Outline each uninfected red blood cell.
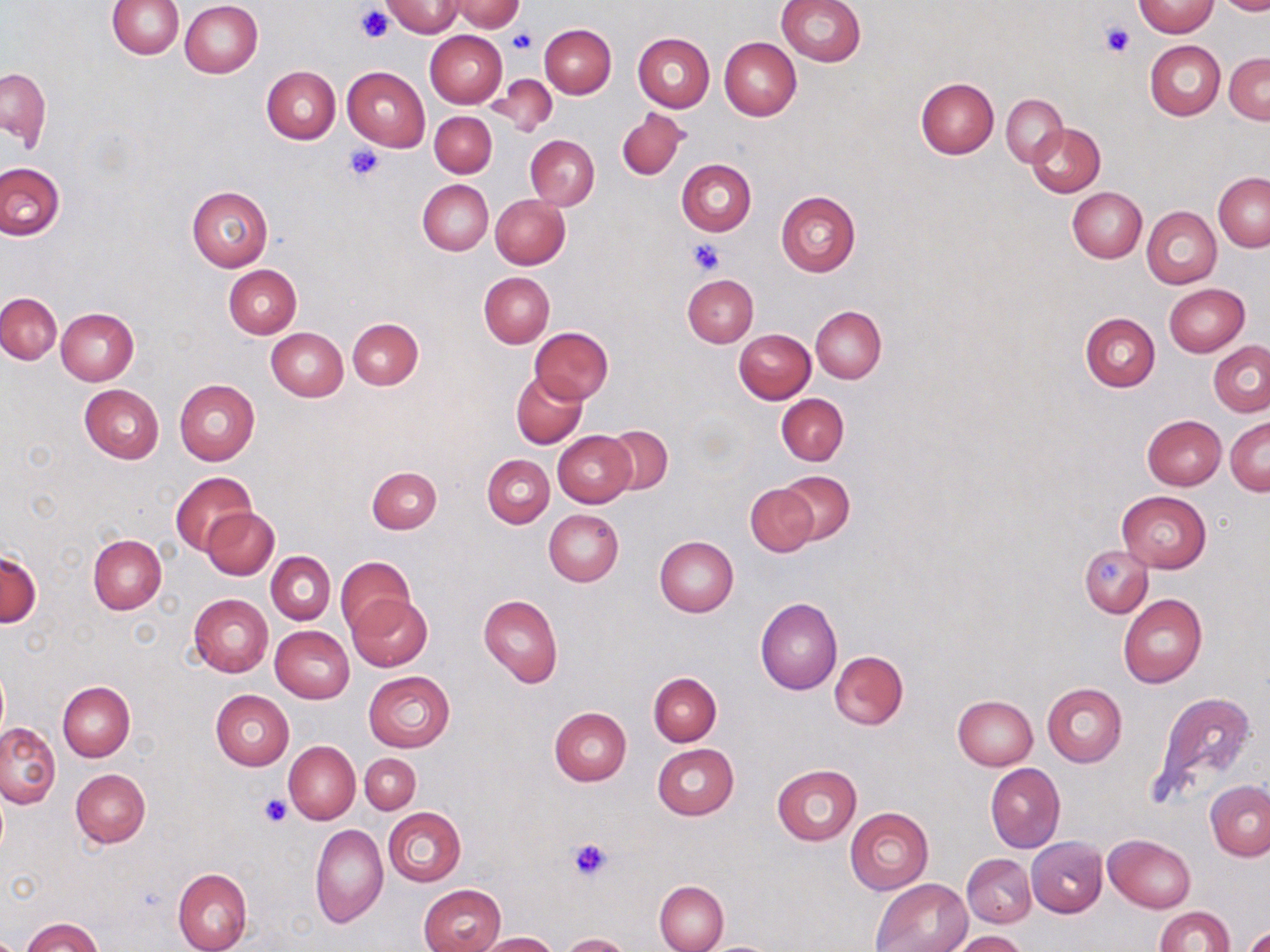

Approximate bounding boxes as (x1,y1)-(x2,y2) corner pairs in pixels.
Uninfected red blood cells: (108,0)-(184,59), (776,0)-(866,65), (1213,0)-(1270,15), (180,1)-(263,78), (382,1)-(463,36), (450,1)-(527,32), (1133,2)-(1218,37), (540,23)-(615,97), (424,30)-(506,108), (632,32)-(715,112), (719,38)-(801,120), (1146,41)-(1225,120), (1225,52)-(1270,124), (262,66)-(340,144), (342,66)-(430,151), (1,68)-(50,148), (488,75)-(558,137), (915,77)-(998,158), (1002,93)-(1067,166), (616,108)-(689,180), (429,111)-(496,177), (1028,122)-(1105,196), (526,135)-(599,209), (677,159)-(756,235), (0,162)-(65,240), (1213,173)-(1270,252), (418,180)-(493,255), (187,185)-(273,272), (1067,187)-(1146,263), (776,190)-(861,276), (489,194)-(571,269), (1142,206)-(1222,289), (224,264)-(301,338), (479,271)-(555,348), (682,274)-(758,347), (1164,284)-(1250,357), (0,293)-(61,364), (811,306)-(886,383), (56,307)-(139,384), (1080,312)-(1160,391), (348,318)-(424,390), (530,327)-(612,403), (266,328)-(348,401), (735,329)-(815,403), (1208,340)-(1270,416), (510,372)-(586,448), (174,379)-(260,464), (79,384)-(164,463), (776,393)-(849,465), (1142,414)-(1226,490), (1227,417)-(1269,495), (603,425)-(672,495), (552,431)-(636,507), (482,453)-(555,527), (367,466)-(442,534), (170,471)-(257,556), (778,471)-(854,544), (745,482)-(819,557), (1116,490)-(1211,572), (203,507)-(279,579), (544,509)-(623,586), (88,534)-(166,614), (654,535)-(738,617), (1078,545)-(1154,618), (0,549)-(40,627), (266,551)-(335,625), (335,556)-(416,635), (189,594)-(273,678), (347,594)-(433,671), (478,594)-(562,688), (1118,594)-(1207,688), (755,597)-(842,694), (270,625)-(354,702), (829,650)-(908,730), (0,667)-(8,740), (364,671)-(454,752), (649,672)-(721,745), (58,682)-(134,760), (1042,683)-(1127,766), (210,689)-(294,770), (1146,689)-(1258,808), (953,695)-(1037,770), (550,707)-(632,786), (0,723)-(60,807), (284,740)-(360,824), (653,745)-(738,820), (361,752)-(421,814), (986,762)-(1065,853), (772,764)-(862,845), (71,768)-(150,848), (1205,781)-(1270,860), (384,807)-(465,886), (845,808)-(934,893), (309,824)-(387,927), (1105,835)-(1195,913), (1027,837)-(1107,917), (962,853)-(1036,928), (172,868)-(251,952), (871,878)-(970,952), (655,881)-(729,952), (420,884)-(505,952), (1154,906)-(1236,952), (23,918)-(102,952), (1245,925)-(1270,952), (952,930)-(1027,952), (477,932)-(558,951), (562,933)-(632,952), (703,939)-(784,951).

Platelet locations: (357,5)-(395,43), (1099,21)-(1134,59), (508,30)-(536,54), (343,143)-(386,181), (688,238)-(724,276), (259,794)-(290,827), (568,837)-(613,881). Slide-level diagnosis: no evidence of blood parasites. Single field of view. May-Grünwald-Giemsa stain. Thin blood smear. Captured at 1000x magnification. Image is 1270×952 pixels. Optical microscopy.